State which parasite is depicted.
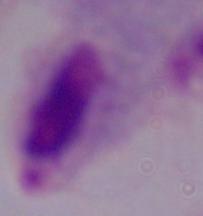

A trichomonad.

{
  "magnification": "1000x",
  "modality": "micrograph"
}